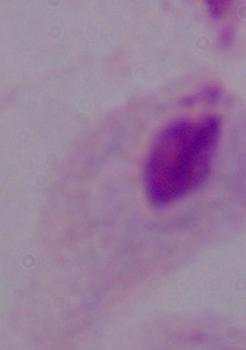

identification: trichomonad
magnification: 1000x
modality: photomicrograph